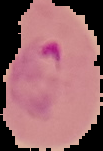
result = Plasmodium parasites identified
image type = cell region segmented out of the field of view; surrounding area masked to black
image size = 103×151 pixels
preparation = thin blood smear